Classify this cell by malaria status.
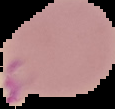

Parasitized.

Segmented cell region on a black background. Image is 115×109 pixels. From a thin blood smear.